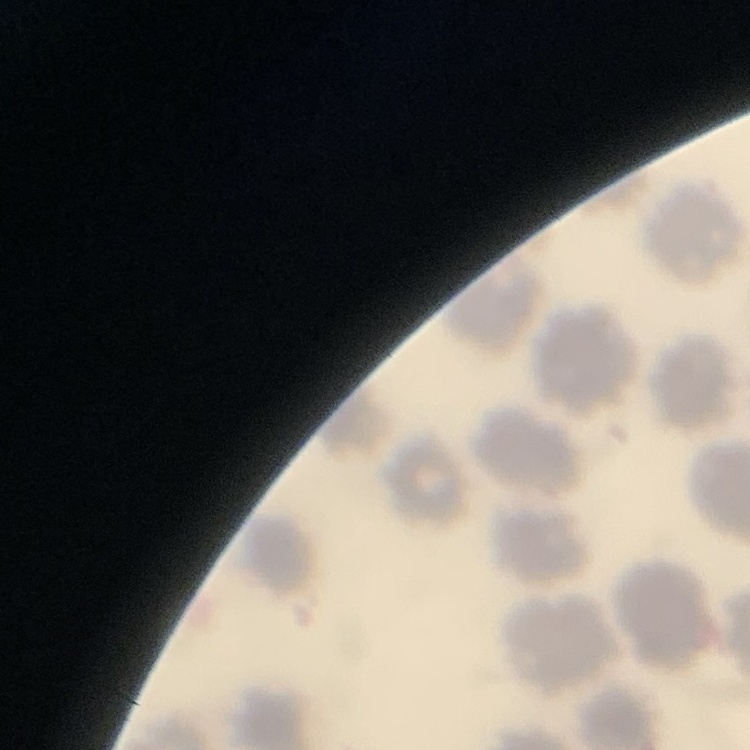
The erythrocytes show no rouleaux formation. Thin peripheral smear. Stained with either Field's or Giemsa. Square crop of a larger photomicrograph.